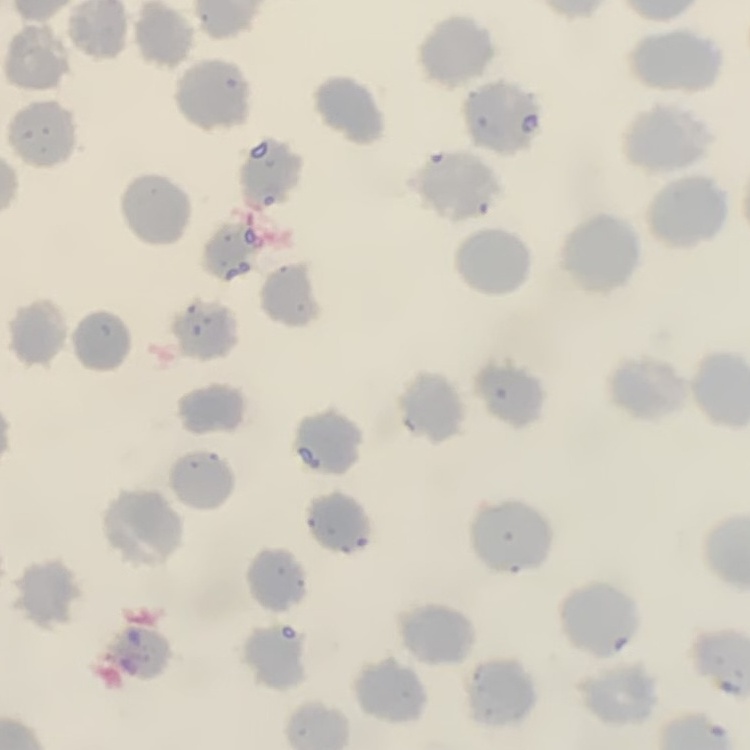

Summary:
  - Red blood cell morphology: no rouleaux formation
  - Stain: Field's or Giemsa
  - Preparation: thin peripheral smear
  - Image type: one tile cut from a larger photomicrograph